Describe the morphology of the red blood cells.
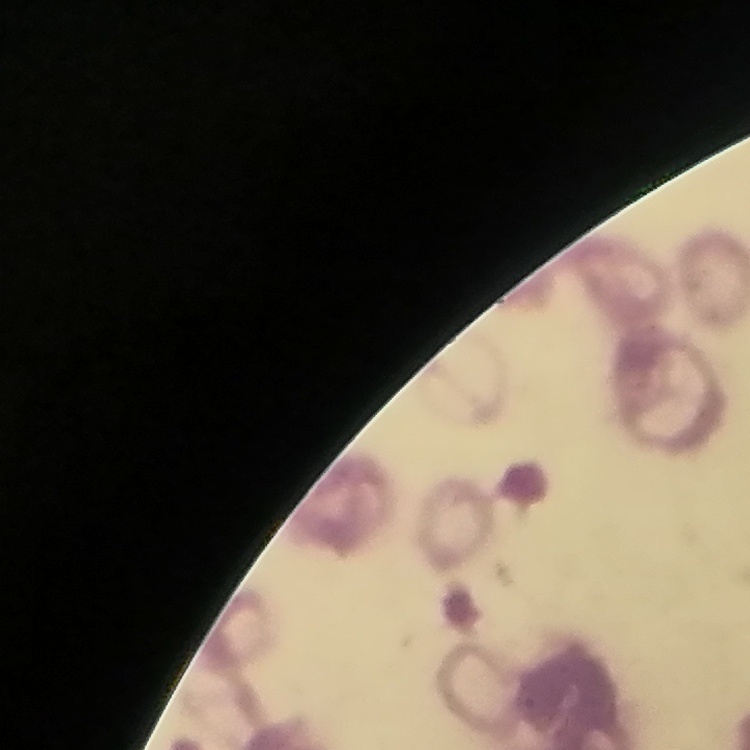
They show rouleaux formation.

One tile cut from a larger photomicrograph. Thin peripheral smear. Stained with either Field's or Giemsa.